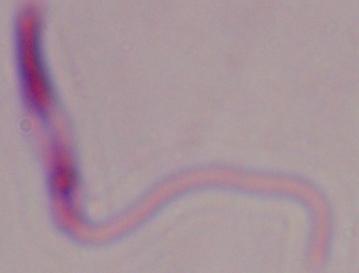
Summary:
  - Identification: Leishmania
  - Magnification: 1000x
  - Modality: micrograph